Give the position of every Plasmodium parasite.
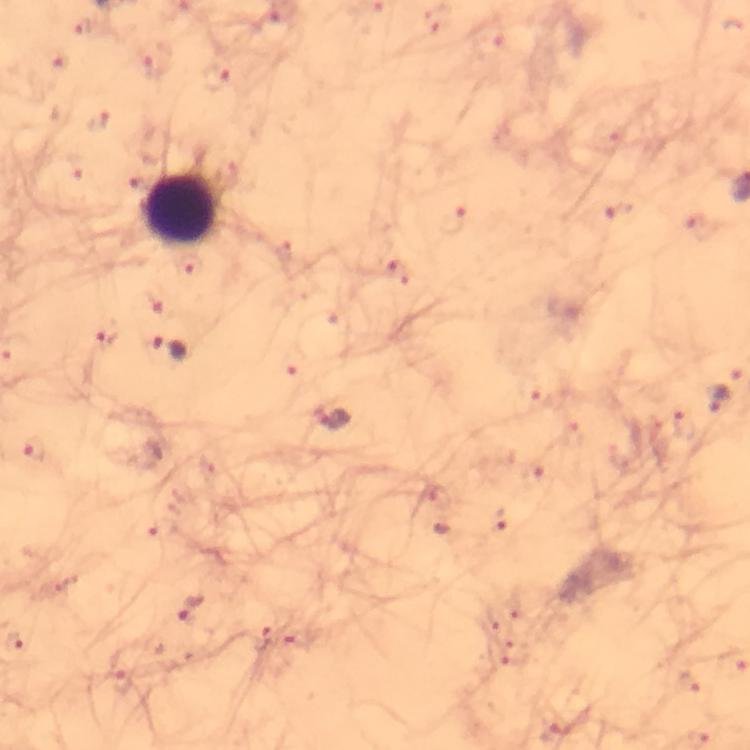

Approximate centers as {x, y} in pixels.
Plasmodium parasites: {212, 77}, {98, 121}, {188, 269}, {107, 336}, {170, 347}, {720, 398}, {336, 420}, {33, 449}, {191, 607}.

immersion_oil: used
capture: smartphone camera through the microscope
image_size: 750×750 pixels
context: from a diagnostic examination for malaria
magnification: 100x
preparation: thick blood film
stain: Giemsa
leukocyte_locations: 'approximate centers as {x, y} in pixels: {180, 208}'
cropped_from: one field of view